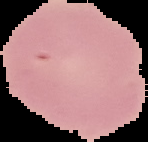

image_size: 148×142 pixels
preparation: thin blood film
image_type: segmented cell region on a black background
result: no Plasmodium parasites seen